Describe the morphology of the red blood cells.
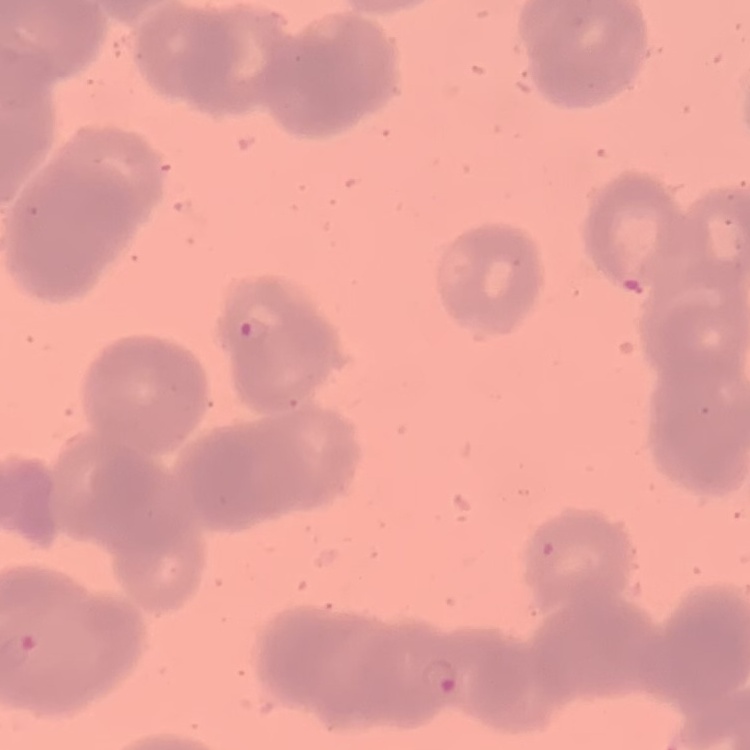
They show rouleaux formation.

Summary:
  - Image type: square crop of a larger photomicrograph
  - Stain: Field's or Giemsa
  - Preparation: thin blood smear